State the blood parasite species.
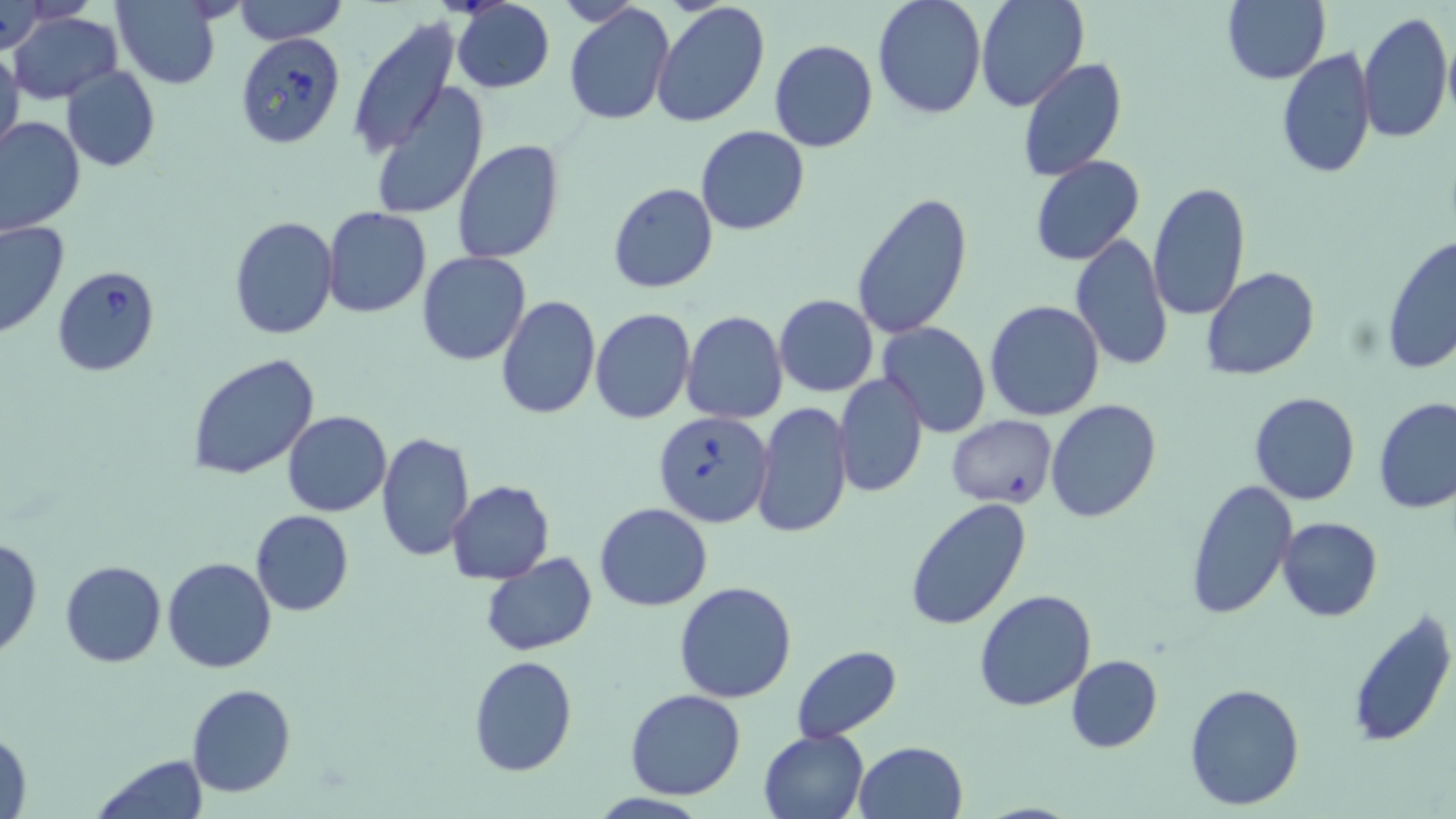

Babesia divergens.

Approximate bounding boxes as [x1, y1, x2, y2] in pixels. Babesia divergens-infected red blood cell locations: [235, 33, 348, 150], [51, 266, 160, 377], [652, 411, 773, 527]. Uninfected red blood cell locations: [234, 0, 347, 44], [872, 0, 987, 121], [975, 0, 1089, 111], [1224, 0, 1331, 85], [451, 1, 556, 94], [111, 2, 221, 88], [650, 2, 771, 129], [2, 3, 48, 55], [564, 5, 675, 125], [1358, 11, 1453, 143], [7, 12, 122, 103], [348, 21, 459, 159], [769, 39, 878, 153], [0, 44, 24, 159], [1277, 47, 1377, 178], [1017, 58, 1127, 180], [61, 64, 160, 172], [370, 85, 489, 221], [0, 116, 85, 236], [695, 125, 810, 236], [451, 140, 564, 264], [1029, 156, 1145, 267], [1146, 181, 1252, 322], [608, 182, 718, 294], [850, 192, 972, 339], [321, 207, 431, 317], [229, 216, 339, 339], [0, 219, 70, 340], [1068, 234, 1172, 375], [1382, 235, 1456, 375], [418, 251, 530, 366], [1200, 266, 1321, 381], [495, 294, 601, 420], [773, 294, 878, 397], [985, 300, 1105, 421], [590, 308, 695, 424], [682, 312, 788, 424], [878, 322, 991, 436], [846, 341, 971, 470], [187, 353, 321, 483], [834, 374, 928, 498], [1249, 392, 1361, 507], [1373, 397, 1456, 515], [1045, 399, 1162, 522], [752, 400, 854, 541], [282, 411, 392, 517], [946, 415, 1057, 509], [374, 430, 475, 561], [1186, 478, 1297, 619], [446, 481, 555, 584], [904, 496, 1033, 633], [594, 503, 713, 611], [250, 510, 354, 616], [1276, 516, 1384, 622], [0, 538, 44, 660], [480, 552, 597, 656], [164, 557, 277, 673], [60, 560, 166, 667], [675, 581, 798, 702], [974, 590, 1097, 712], [1343, 607, 1456, 750], [790, 646, 902, 741], [468, 655, 577, 775], [1067, 655, 1163, 753], [1184, 681, 1306, 812], [186, 684, 295, 799], [625, 688, 746, 800], [1, 725, 33, 819], [758, 729, 869, 819], [853, 741, 968, 819], [91, 754, 210, 819]. Thin blood smear. Light microscopy. May-Grünwald-Giemsa-stained preparation. Image is 1456×819 pixels. Captured at 1000x magnification. One field of a larger specimen.